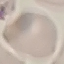

Summary:
  - Result: no malaria parasites detected
  - Capture: smartphone camera at the microscope eyepiece
  - Stain: Giemsa
  - Preparation: thin smear
  - Image type: automatically extracted cell patch, resized to 64 × 64 pixels